Identify the preparation type.
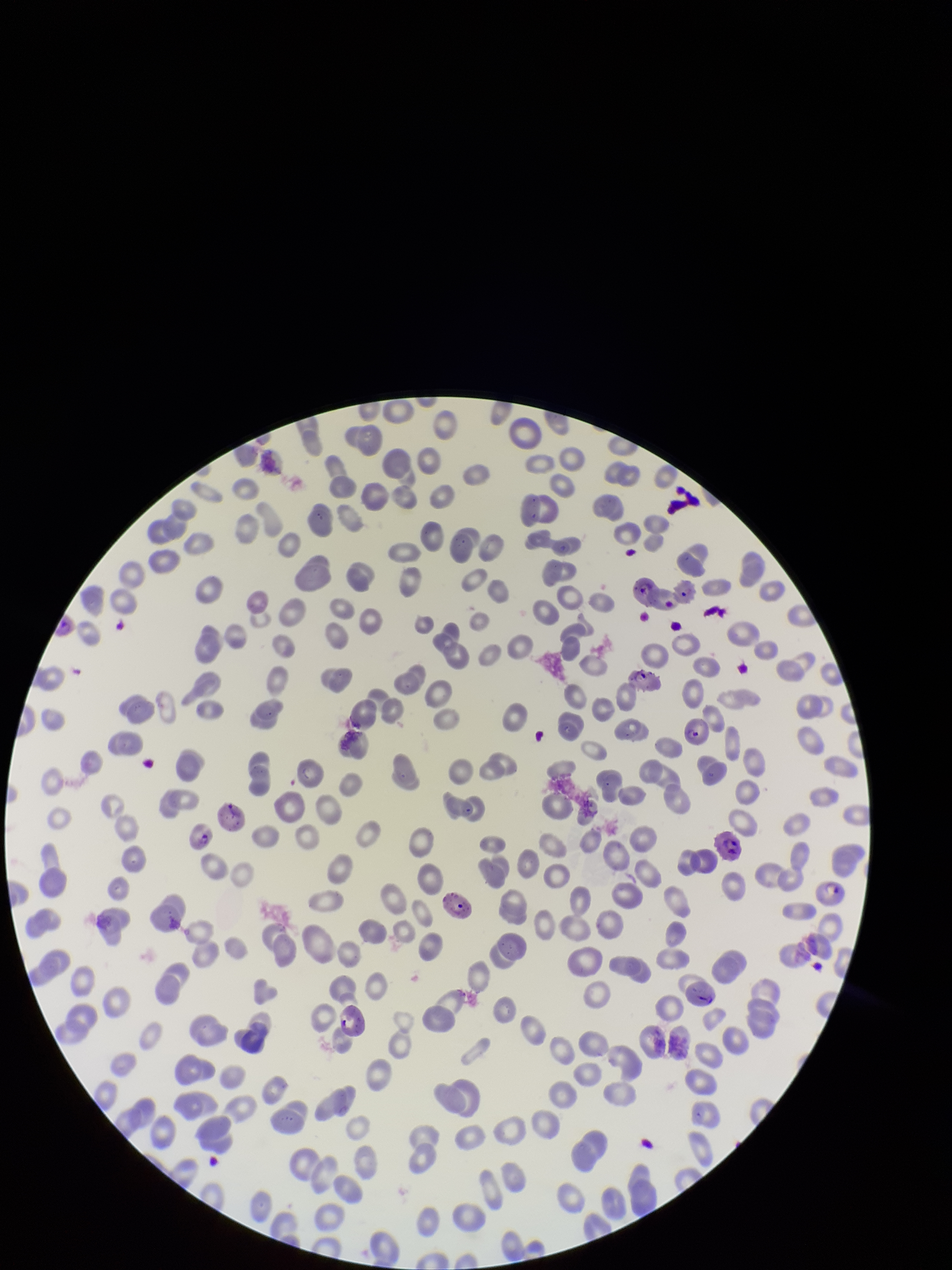

A thin smear.

field of view = one from this slide
species reported for this patient = Plasmodium falciparum
image size = 952×1270 pixels
stain = Giemsa
parasitized red blood cells = seen
capture = smartphone photograph through the microscope eyepiece
patient malaria status = positive
parasitized red blood cell count = 15
red blood cell count = 247